Give the extent of all uninfected red blood cells.
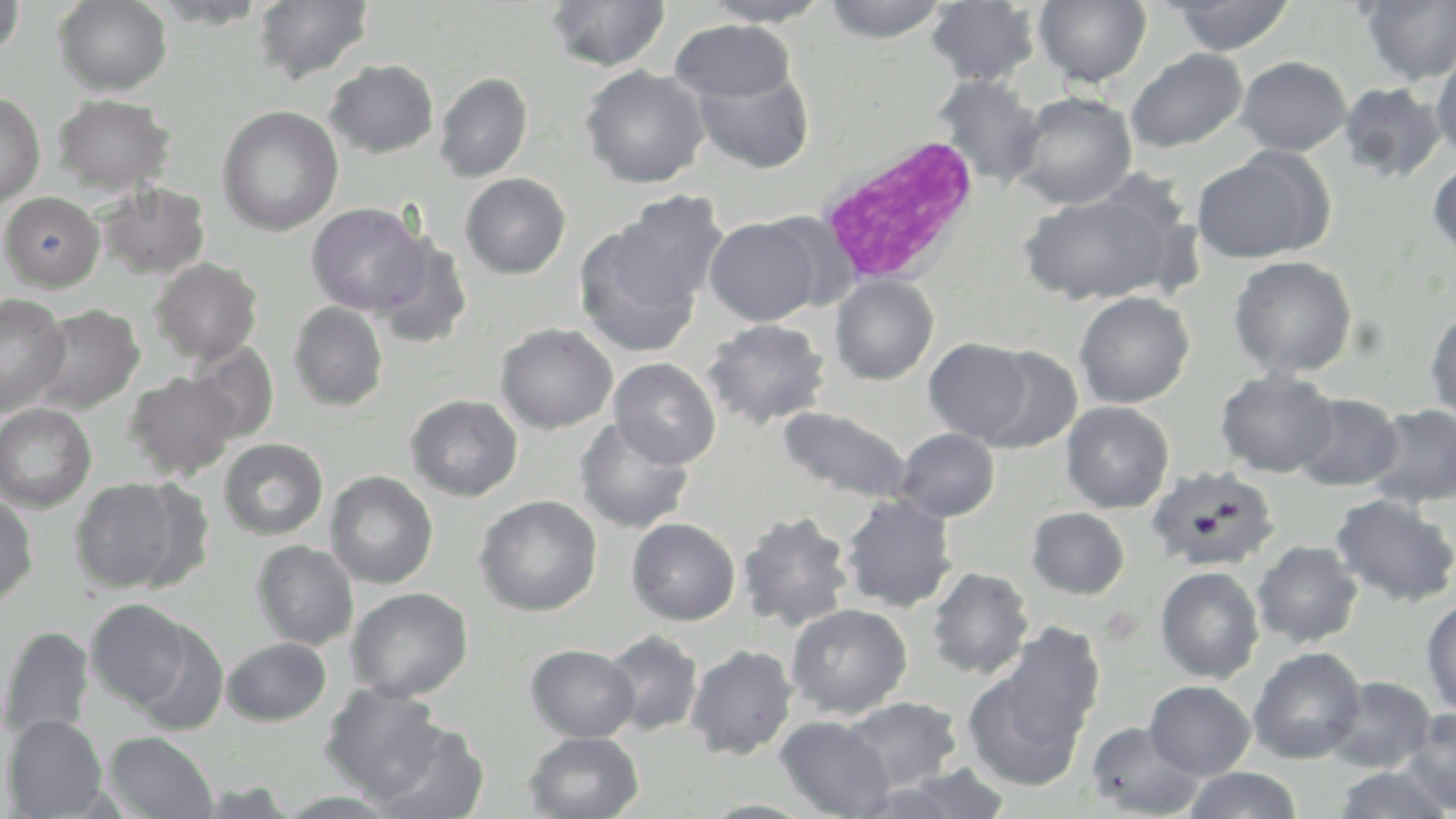
Approximate bounding boxes as (x1,y1)-(x2,y2) corner pairs in pixels.
Uninfected red blood cells: (0,0)-(24,60), (55,0)-(172,95), (147,0)-(273,28), (545,0)-(670,73), (698,0)-(833,26), (821,0)-(952,42), (1035,0)-(1152,87), (1168,0)-(1295,55), (254,1)-(373,84), (926,1)-(1042,87), (1359,1)-(1456,85), (670,20)-(795,104), (1431,47)-(1456,162), (1125,48)-(1248,152), (1235,56)-(1351,155), (324,59)-(439,158), (580,66)-(708,189), (692,66)-(814,174), (434,72)-(533,182), (932,74)-(1045,187), (1337,82)-(1447,183), (1011,91)-(1137,210), (0,92)-(45,209), (52,93)-(176,196), (216,105)-(343,235), (1191,150)-(1328,262), (1427,159)-(1456,259), (460,172)-(571,279), (1016,176)-(1193,308), (96,182)-(211,281), (1,191)-(104,291), (604,191)-(728,319), (306,202)-(429,316), (704,215)-(825,326), (574,220)-(707,357), (371,234)-(473,349), (1229,255)-(1357,378), (150,257)-(263,365), (830,275)-(938,385), (1074,291)-(1195,408), (0,294)-(71,415), (289,301)-(388,411), (29,304)-(144,414), (1425,307)-(1456,424), (704,319)-(829,429), (495,323)-(618,434), (924,337)-(1035,445), (187,341)-(279,445), (977,345)-(1083,453), (609,357)-(721,468), (1215,368)-(1340,477), (125,371)-(241,481), (1292,392)-(1403,491), (406,394)-(523,501), (1061,401)-(1174,513), (0,403)-(97,512), (1365,403)-(1456,508), (777,407)-(912,503), (574,417)-(695,533), (894,428)-(1000,521), (218,438)-(328,540), (1147,465)-(1281,573), (324,471)-(438,589), (69,477)-(200,595), (1330,493)-(1455,607), (0,494)-(38,607), (839,494)-(957,613), (475,495)-(602,616), (1026,507)-(1130,599), (737,510)-(854,632), (627,517)-(741,626), (252,540)-(358,650), (1252,540)-(1364,647), (926,566)-(1034,679), (1155,566)-(1265,683), (347,587)-(473,702), (1421,597)-(1456,718), (85,598)-(195,711), (786,603)-(912,719), (131,621)-(229,736), (999,624)-(1106,744), (0,625)-(95,742), (601,630)-(703,737), (222,638)-(331,726), (526,644)-(640,742), (686,644)-(798,759), (1247,646)-(1367,764), (963,669)-(1088,791), (1324,676)-(1435,774), (1144,680)-(1256,779), (319,683)-(450,803), (840,697)-(962,793), (1401,708)-(1456,814), (2,714)-(108,818), (775,715)-(894,819), (1085,720)-(1206,818), (370,722)-(489,819), (103,731)-(218,818), (524,731)-(644,819), (863,765)-(1013,818), (1331,765)-(1454,818), (1183,767)-(1303,819), (274,790)-(403,818), (696,799)-(821,818).

slide-level diagnosis = negative for blood parasites
image size = 1456×819 pixels
field of view = single
modality = optical microscopy
white blood cell locations = approximate bounding boxes as (x1,y1)-(x2,y2) corner pairs in pixels: (818,134)-(981,287)
stain = May-Grünwald-Giemsa
preparation = thin blood film
magnification = 1000x